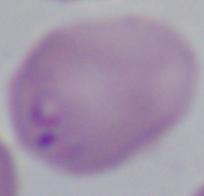

identification = Babesia
modality = micrograph
magnification = 1000x